Name the blood parasite species.
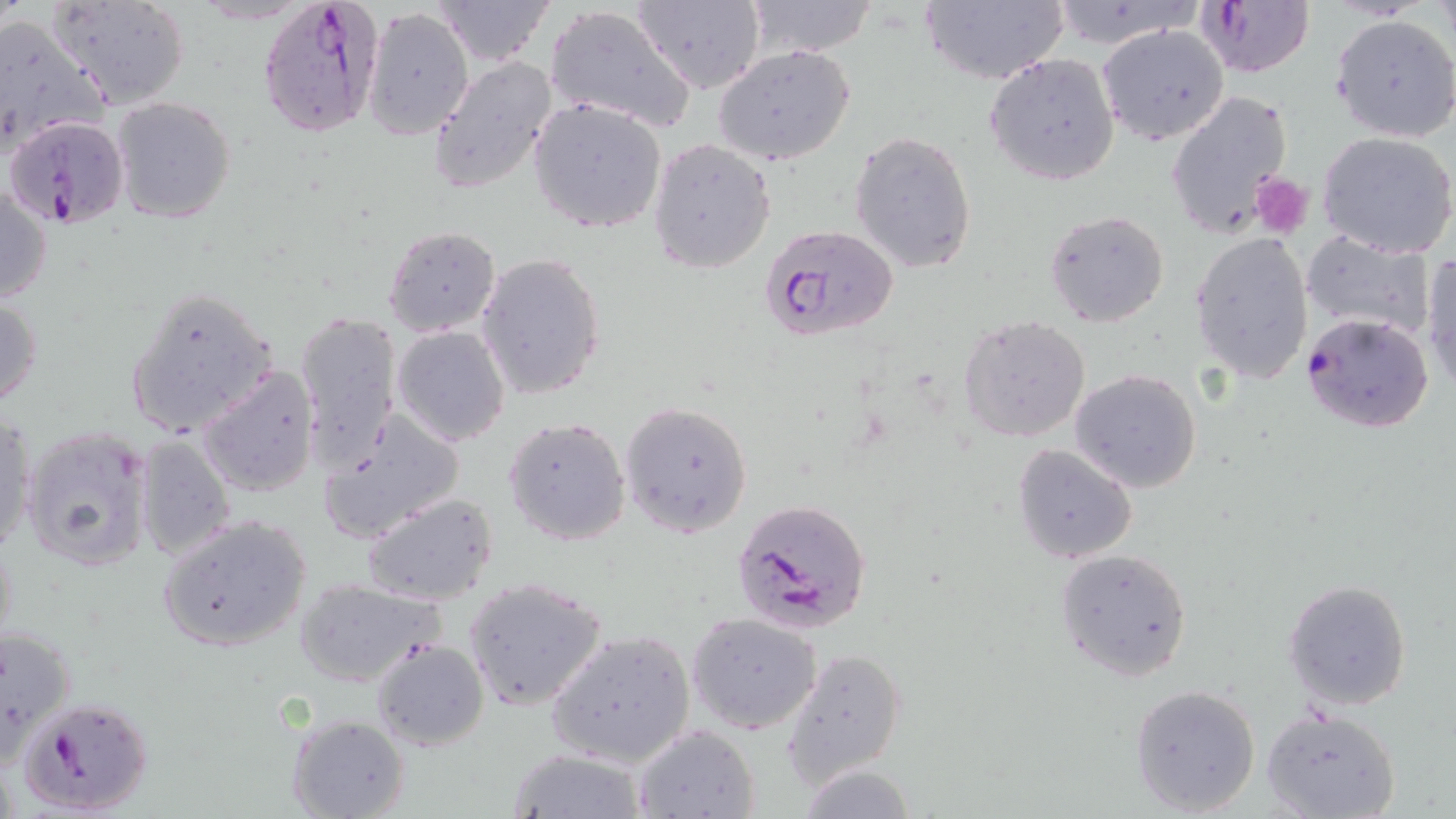
Plasmodium falciparum.

Summary:
  - Coordinate format: approximate bounding boxes as named x1/y1/x2/y2 corners in pixels
  - Platelet locations: (x1=1250, y1=174, x2=1314, y2=238)
  - Plasmodium falciparum-infected red blood cell locations: (x1=258, y1=0, x2=386, y2=138), (x1=1195, y1=2, x2=1316, y2=79), (x1=4, y1=115, x2=130, y2=228), (x1=758, y1=224, x2=899, y2=342), (x1=1301, y1=310, x2=1436, y2=433), (x1=732, y1=497, x2=871, y2=635), (x1=20, y1=696, x2=153, y2=814)
  - Uninfected red blood cell locations: (x1=48, y1=0, x2=193, y2=110), (x1=429, y1=0, x2=556, y2=67), (x1=632, y1=0, x2=766, y2=93), (x1=744, y1=0, x2=877, y2=57), (x1=918, y1=0, x2=1069, y2=87), (x1=1041, y1=1, x2=1204, y2=52), (x1=544, y1=3, x2=696, y2=133), (x1=363, y1=7, x2=475, y2=141), (x1=0, y1=14, x2=108, y2=154), (x1=1330, y1=14, x2=1456, y2=142), (x1=1098, y1=25, x2=1229, y2=144), (x1=714, y1=45, x2=856, y2=167), (x1=983, y1=53, x2=1121, y2=186), (x1=429, y1=56, x2=560, y2=196), (x1=1164, y1=88, x2=1292, y2=235), (x1=110, y1=95, x2=237, y2=224), (x1=528, y1=98, x2=668, y2=235), (x1=849, y1=129, x2=978, y2=274), (x1=1317, y1=131, x2=1456, y2=258), (x1=648, y1=138, x2=775, y2=274), (x1=0, y1=181, x2=52, y2=307), (x1=1043, y1=209, x2=1171, y2=327), (x1=382, y1=225, x2=502, y2=337), (x1=1302, y1=229, x2=1437, y2=342), (x1=1190, y1=231, x2=1314, y2=384), (x1=476, y1=253, x2=605, y2=401), (x1=1423, y1=254, x2=1456, y2=392), (x1=125, y1=285, x2=276, y2=438), (x1=0, y1=295, x2=43, y2=410), (x1=296, y1=310, x2=401, y2=473), (x1=959, y1=315, x2=1091, y2=443), (x1=392, y1=324, x2=510, y2=446), (x1=198, y1=364, x2=320, y2=497), (x1=1069, y1=369, x2=1203, y2=494), (x1=619, y1=400, x2=753, y2=538), (x1=320, y1=411, x2=465, y2=545), (x1=1, y1=412, x2=36, y2=559), (x1=503, y1=417, x2=633, y2=545), (x1=22, y1=427, x2=151, y2=570), (x1=135, y1=435, x2=237, y2=561), (x1=1013, y1=443, x2=1138, y2=565), (x1=137, y1=457, x2=270, y2=633), (x1=362, y1=491, x2=499, y2=606), (x1=159, y1=513, x2=314, y2=655), (x1=1054, y1=547, x2=1193, y2=681), (x1=294, y1=578, x2=446, y2=686), (x1=461, y1=578, x2=607, y2=711), (x1=1281, y1=578, x2=1413, y2=711), (x1=687, y1=612, x2=823, y2=734), (x1=0, y1=624, x2=78, y2=755), (x1=547, y1=631, x2=696, y2=766), (x1=371, y1=639, x2=488, y2=751), (x1=783, y1=648, x2=907, y2=789), (x1=1127, y1=683, x2=1262, y2=815), (x1=1261, y1=705, x2=1402, y2=819), (x1=286, y1=714, x2=408, y2=819), (x1=632, y1=724, x2=760, y2=818), (x1=505, y1=748, x2=648, y2=818)
  - Field of view: one of a larger specimen
  - Magnification: 1000x
  - Image size: 1456×819 pixels
  - Modality: optical microscopy
  - Preparation: thin blood film
  - Stain: May-Grünwald-Giemsa